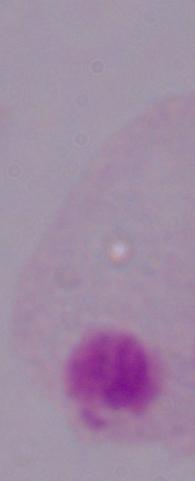
Micrograph. Captured at 1000x magnification. A trichomonad is shown.